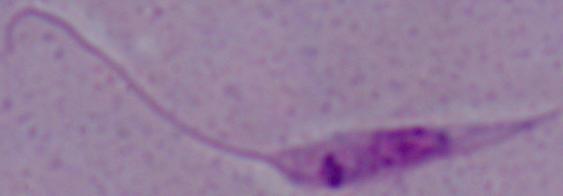
modality: micrograph
identification: Leishmania
magnification: 1000x